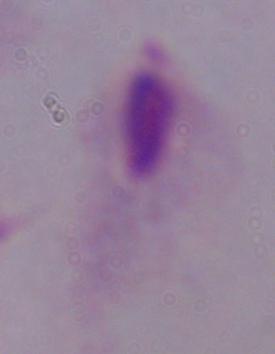
{
  "modality": "photomicrograph",
  "identification": "trichomonad",
  "magnification": "1000x"
}